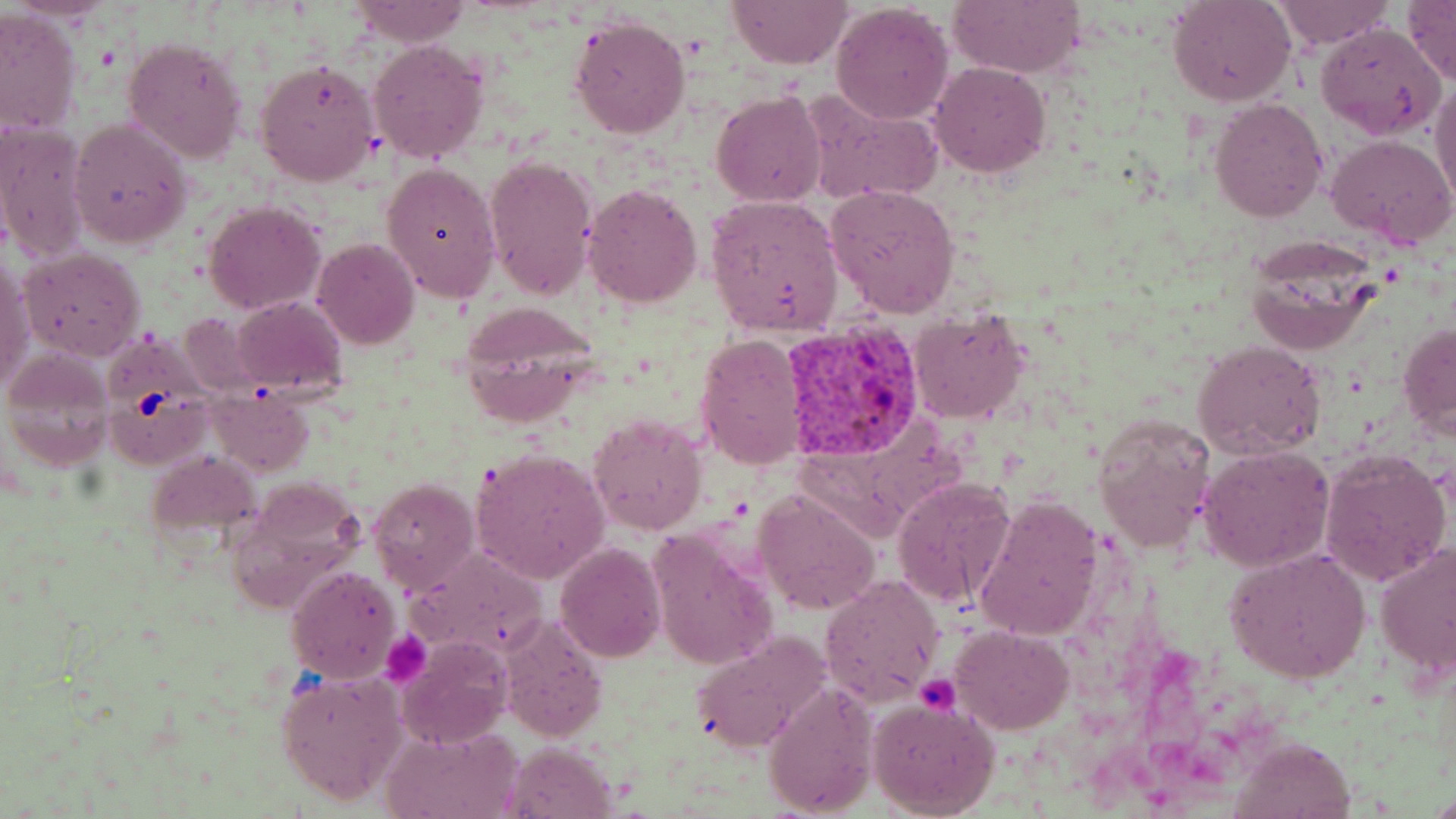

Summary:
  - Coordinate format: approximate bounding boxes as (x1,y1)-(x2,y2) corner pairs in pixels
  - Uninfected red blood cell locations: (350,0)-(473,47), (728,0)-(852,68), (947,0)-(1084,77), (1168,0)-(1296,107), (1271,1)-(1393,49), (1401,1)-(1455,86), (830,4)-(952,123), (0,8)-(82,138), (569,15)-(690,138), (1318,23)-(1444,141), (124,36)-(248,163), (369,38)-(489,164), (256,61)-(380,185), (931,63)-(1051,178), (1430,79)-(1456,207), (800,87)-(945,206), (712,92)-(826,208), (1208,98)-(1327,222), (71,118)-(192,248), (0,123)-(91,263), (1327,135)-(1456,250), (483,154)-(597,300), (382,162)-(502,302), (583,184)-(701,307), (826,184)-(961,320), (704,195)-(845,338), (204,202)-(325,313), (314,239)-(420,350), (1243,239)-(1383,354), (18,246)-(147,363), (1,255)-(34,394), (231,296)-(347,394), (462,307)-(597,431), (909,310)-(1031,424), (181,312)-(267,397), (1398,324)-(1456,437), (97,325)-(214,473), (695,333)-(807,469), (1195,340)-(1326,457), (2,348)-(115,473), (207,387)-(315,476), (1091,412)-(1217,554), (589,413)-(707,535), (1198,445)-(1335,571), (469,447)-(610,584), (1320,449)-(1451,586), (146,452)-(260,546), (892,476)-(1016,607), (368,478)-(478,594), (753,488)-(880,614), (972,497)-(1103,640), (646,527)-(778,673), (556,543)-(666,661), (1375,543)-(1456,678), (412,547)-(546,657), (1225,548)-(1372,684), (286,565)-(401,683), (821,574)-(944,705), (500,616)-(609,739), (950,626)-(1075,732), (689,632)-(829,754), (397,635)-(511,748), (276,669)-(408,805), (765,679)-(878,817), (868,696)-(1002,819), (382,725)-(520,819), (1233,737)-(1353,818), (507,741)-(617,818)
  - Platelet locations: (381,631)-(433,686), (915,674)-(960,715)
  - Plasmodium vivax-infected red blood cell locations: (782,320)-(926,462)
  - Slide-level diagnosis: Plasmodium vivax
  - Modality: optical microscopy
  - Stain: May-Grünwald-Giemsa
  - Image size: 1456×819 pixels
  - Field of view: one of a larger specimen
  - Magnification: 1000x
  - Preparation: thin blood film